Name the parasite shown.
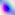

Toxoplasma gondii.

Summary:
  - Modality: micrograph
  - Magnification: 400x